Locate every white blood cell.
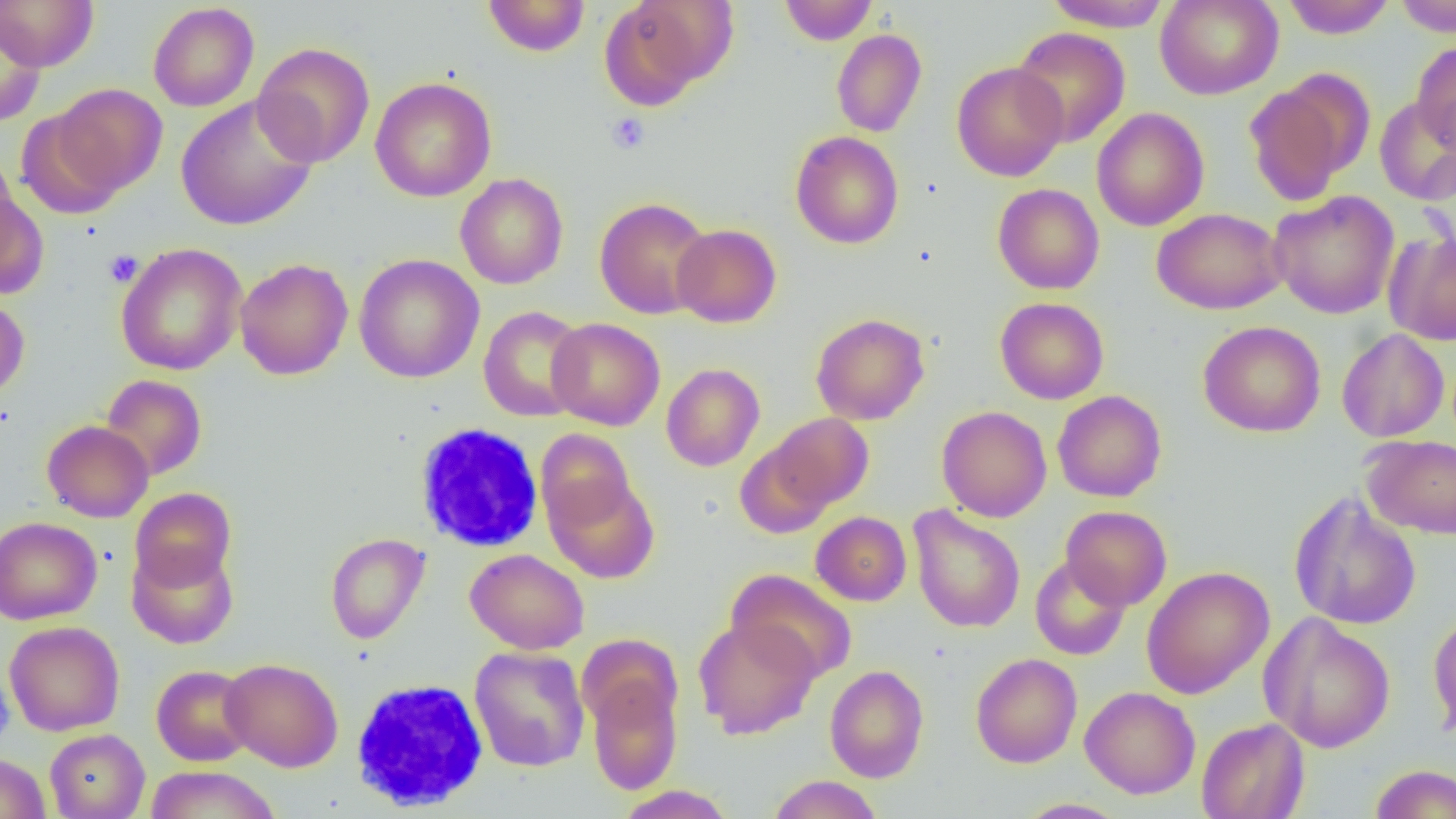
Approximate bounding boxes as (x1,y1)-(x2,y2) corner pairs in pixels.
White blood cells: (413,422)-(544,552), (348,678)-(490,812).

Summary:
  - Uninfected red blood cell locations: (0,0)-(99,70), (483,0)-(590,57), (599,0)-(730,108), (778,0)-(877,45), (1042,0)-(1174,31), (1155,0)-(1283,100), (1281,0)-(1397,39), (1394,0)-(1456,37), (148,2)-(260,111), (0,12)-(46,128), (1011,26)-(1130,147), (831,29)-(927,138), (252,41)-(375,167), (1411,42)-(1456,152), (951,61)-(1068,181), (1244,75)-(1370,205), (370,76)-(497,202), (50,84)-(168,197), (176,95)-(318,231), (1374,96)-(1456,206), (1092,107)-(1209,231), (16,108)-(126,219), (790,131)-(904,249), (455,173)-(568,289), (0,181)-(48,299), (992,183)-(1104,295), (1268,190)-(1400,319), (594,197)-(714,319), (1152,207)-(1287,315), (671,223)-(781,328), (1385,230)-(1456,345), (115,243)-(247,375), (354,253)-(485,384), (234,258)-(353,380), (0,294)-(30,400), (995,297)-(1109,404), (478,306)-(589,422), (811,313)-(929,425), (546,317)-(665,430), (1198,320)-(1326,437), (1336,329)-(1450,442), (661,363)-(765,471), (100,374)-(207,481), (1052,390)-(1167,503), (937,406)-(1052,522), (769,412)-(874,511), (42,420)-(154,522), (415,423)-(547,553), (535,428)-(636,532), (1362,434)-(1456,539), (734,441)-(834,539), (545,475)-(659,583), (129,487)-(236,589), (1288,492)-(1422,630), (907,505)-(1026,634), (1060,505)-(1172,610), (810,511)-(912,606), (0,516)-(102,625), (325,532)-(430,644), (127,542)-(238,649), (465,548)-(590,654), (1030,556)-(1131,660), (1141,566)-(1274,699), (727,569)-(857,682), (1428,609)-(1456,740), (1260,613)-(1396,753), (693,617)-(820,739), (4,621)-(125,736), (576,633)-(683,734), (469,646)-(590,772), (970,652)-(1082,768), (220,658)-(343,772), (824,664)-(929,782), (151,665)-(256,766), (0,666)-(13,752), (586,673)-(683,795), (347,674)-(494,811), (1080,686)-(1200,799), (1196,718)-(1309,819), (45,729)-(150,819), (0,753)-(50,819), (1369,764)-(1456,818), (145,765)-(282,819), (767,775)-(883,819), (615,785)-(735,818), (1015,798)-(1131,818)
  - Platelet locations: (605,112)-(650,154), (104,249)-(143,287)
  - Slide-level diagnosis: no evidence of blood parasites
  - Image size: 1456×819 pixels
  - Magnification: 1000x
  - Preparation: thin blood smear
  - Field of view: single
  - Modality: light microscopy